Outline each blood parasite and name the species.
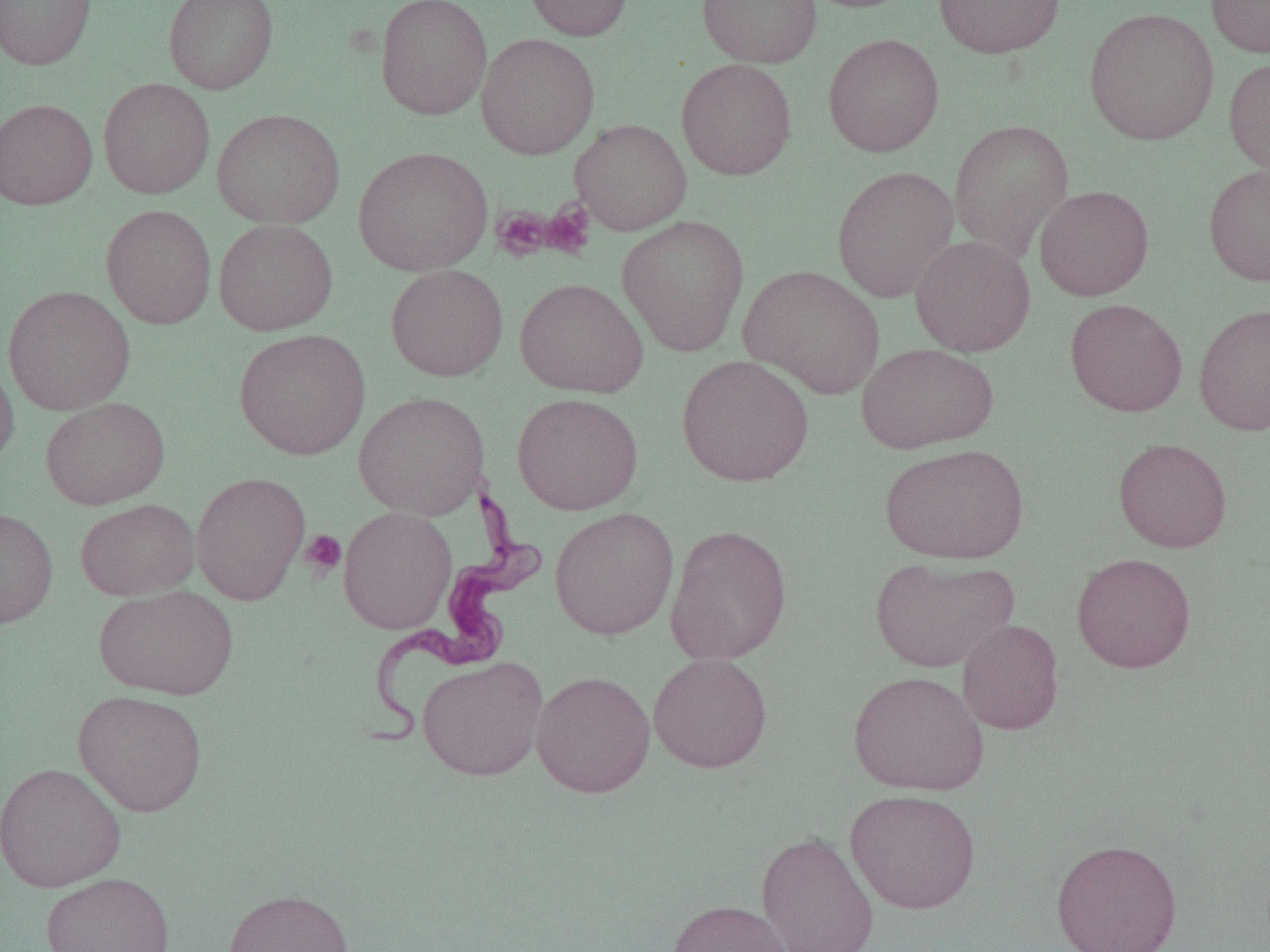
Approximate bounding boxes as (x1,y1)-(x2,y2) corner pairs in pixels.
Trypanosoma brucei: (358,485)-(547,747).
No Plasmodium falciparum, Plasmodium ovale, Plasmodium malariae, Plasmodium vivax, or Babesia divergens observed.

{
  "slide_level_diagnosis": "Trypanosoma brucei",
  "uninfected_red_blood_cell_locations": "approximate bounding boxes as (x1,y1)-(x2,y2) corner pairs in pixels: (0,0)-(96,69), (163,0)-(279,94), (375,0)-(492,120), (525,0)-(633,41), (697,0)-(822,68), (798,0)-(921,13), (933,0)-(1065,59), (1206,0)-(1270,58), (1084,7)-(1219,145), (476,33)-(599,160), (823,33)-(944,157), (1224,56)-(1270,181), (676,58)-(797,180), (98,77)-(215,199), (0,98)-(98,210), (212,108)-(346,228), (570,119)-(692,235), (948,119)-(1074,261), (353,146)-(493,276), (1203,163)-(1270,286), (831,165)-(959,302), (1035,185)-(1154,301), (101,204)-(216,329), (617,215)-(749,356), (213,219)-(338,335), (910,235)-(1035,357), (386,264)-(508,381), (740,264)-(886,398), (515,278)-(648,397), (3,285)-(135,415), (1065,299)-(1187,417), (1193,302)-(1270,437), (234,328)-(371,461), (856,342)-(998,454), (0,355)-(19,470), (676,355)-(814,486), (354,391)-(490,520), (511,393)-(644,515), (40,397)-(170,509), (1113,438)-(1232,552), (880,443)-(1029,564), (191,471)-(311,605), (76,498)-(199,601), (338,506)-(457,634), (549,507)-(679,640), (0,508)-(58,628), (665,524)-(792,666), (1072,552)-(1196,673), (870,556)-(1018,672), (94,586)-(238,699), (957,619)-(1064,735), (648,652)-(773,773), (416,655)-(548,781), (531,670)-(655,797), (848,670)-(989,796), (73,690)-(207,817), (0,762)-(127,892), (845,789)-(981,914), (756,829)-(879,952), (1051,838)-(1182,952), (40,872)-(175,952), (222,888)-(354,952), (667,900)-(792,952)",
  "field_of_view": "single",
  "platelet_locations": "approximate bounding boxes as (x1,y1)-(x2,y2) corner pairs in pixels: (541,202)-(595,259), (492,206)-(553,261), (300,530)-(347,578)",
  "image_size": "1270×952 pixels",
  "modality": "light microscopy",
  "magnification": "1000x",
  "preparation": "thin blood film"
}